Classify this cell by malaria status.
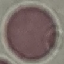

Uninfected.

{
  "preparation": "thin blood film",
  "capture": "smartphone camera at the microscope eyepiece",
  "stain": "Giemsa",
  "image_type": "cell patch, automatically extracted from a larger field of view and resized to 64 × 64 pixels"
}